Name the parasite shown.
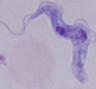
A trypanosome.

{
  "modality": "micrograph",
  "magnification": "1000x"
}